Report the malaria status of this cell.
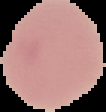
It is uninfected.

Image is 106×112 pixels. The area outside the segmented cell region is set to black. From a thin blood film.